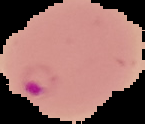

Summary:
  - Image size: 145×124 pixels
  - Malaria status: parasitized
  - Image type: cell region segmented out of the field of view; surrounding area masked to black
  - Preparation: thin blood smear